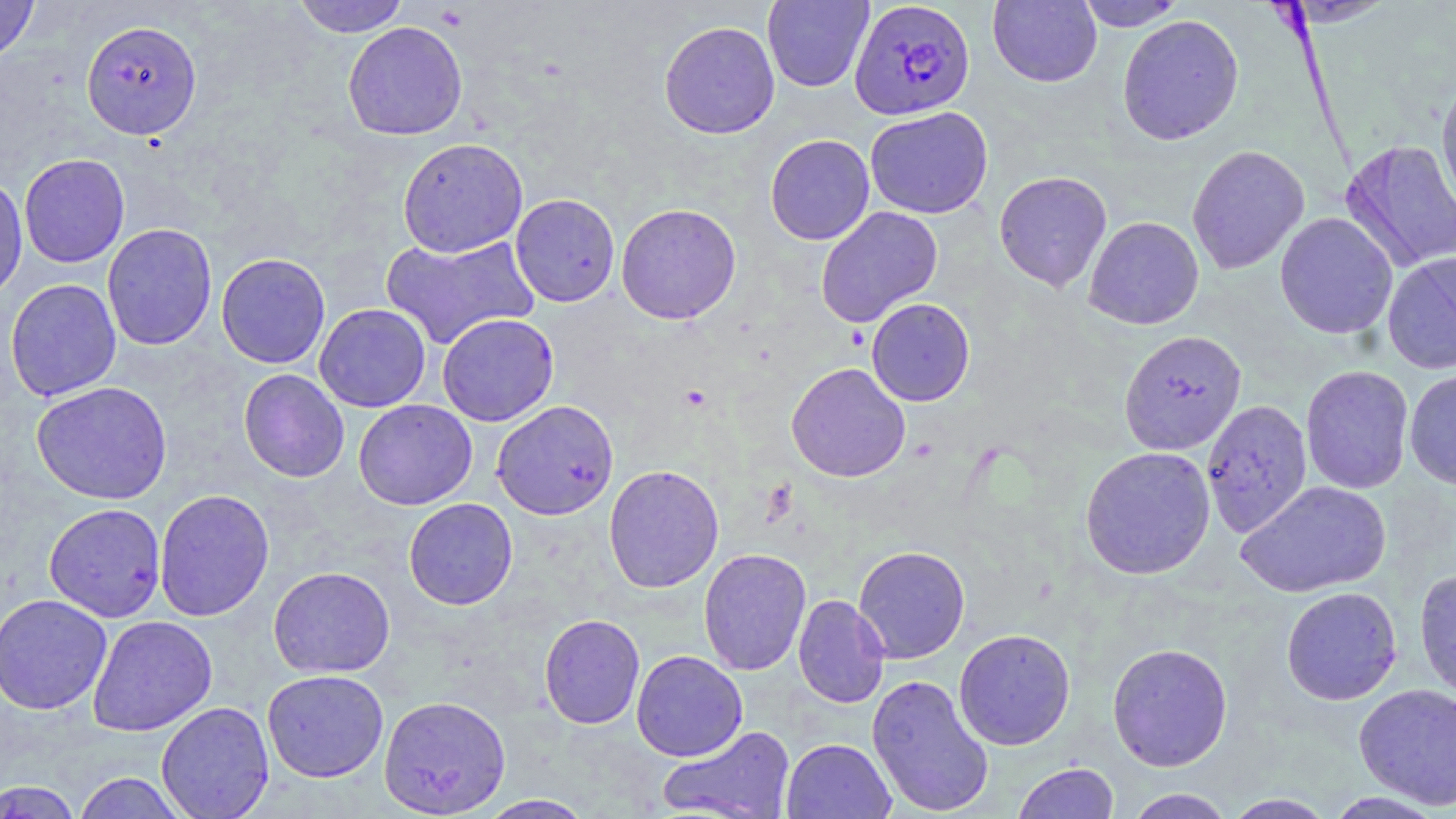
Summary:
  - Coordinate format: approximate bounding boxes as named x1/y1/x2/y2 corners in pixels
  - Plasmodium falciparum-infected red blood cell locations: (x1=849, y1=1, x2=976, y2=120)
  - Uninfected red blood cell locations: (x1=0, y1=0, x2=39, y2=66), (x1=292, y1=0, x2=410, y2=37), (x1=762, y1=0, x2=873, y2=92), (x1=1075, y1=0, x2=1187, y2=31), (x1=987, y1=1, x2=1101, y2=88), (x1=1281, y1=1, x2=1397, y2=27), (x1=1117, y1=15, x2=1244, y2=145), (x1=81, y1=20, x2=202, y2=140), (x1=342, y1=21, x2=468, y2=141), (x1=659, y1=21, x2=780, y2=139), (x1=1436, y1=75, x2=1456, y2=216), (x1=865, y1=106, x2=993, y2=219), (x1=765, y1=134, x2=875, y2=245), (x1=397, y1=137, x2=528, y2=258), (x1=1341, y1=139, x2=1456, y2=272), (x1=1187, y1=144, x2=1309, y2=274), (x1=19, y1=153, x2=130, y2=268), (x1=993, y1=171, x2=1112, y2=292), (x1=0, y1=174, x2=28, y2=301), (x1=510, y1=193, x2=621, y2=307), (x1=616, y1=203, x2=741, y2=324), (x1=815, y1=206, x2=943, y2=327), (x1=1274, y1=212, x2=1398, y2=339), (x1=1084, y1=216, x2=1204, y2=330), (x1=101, y1=223, x2=217, y2=350), (x1=379, y1=233, x2=540, y2=350), (x1=215, y1=252, x2=331, y2=369), (x1=1382, y1=252, x2=1456, y2=374), (x1=5, y1=278, x2=122, y2=402), (x1=866, y1=298, x2=975, y2=406), (x1=314, y1=303, x2=431, y2=412), (x1=436, y1=313, x2=559, y2=426), (x1=1119, y1=330, x2=1246, y2=455), (x1=786, y1=362, x2=910, y2=482), (x1=1300, y1=365, x2=1414, y2=494), (x1=1404, y1=368, x2=1456, y2=490), (x1=238, y1=369, x2=349, y2=483), (x1=31, y1=381, x2=173, y2=505), (x1=1201, y1=399, x2=1312, y2=538), (x1=353, y1=400, x2=477, y2=510), (x1=491, y1=400, x2=619, y2=520), (x1=1080, y1=446, x2=1215, y2=580), (x1=603, y1=465, x2=724, y2=593), (x1=1235, y1=480, x2=1392, y2=599), (x1=154, y1=489, x2=275, y2=621), (x1=403, y1=498, x2=518, y2=610), (x1=44, y1=502, x2=166, y2=621), (x1=853, y1=545, x2=970, y2=663), (x1=698, y1=547, x2=812, y2=676), (x1=268, y1=566, x2=395, y2=678), (x1=1414, y1=566, x2=1456, y2=701), (x1=1280, y1=587, x2=1403, y2=705), (x1=0, y1=593, x2=112, y2=715), (x1=793, y1=594, x2=889, y2=709), (x1=539, y1=613, x2=645, y2=729), (x1=87, y1=615, x2=217, y2=736), (x1=953, y1=628, x2=1075, y2=750), (x1=1107, y1=642, x2=1233, y2=771), (x1=631, y1=650, x2=747, y2=761), (x1=262, y1=669, x2=389, y2=782), (x1=867, y1=674, x2=994, y2=816), (x1=1353, y1=683, x2=1456, y2=809), (x1=379, y1=695, x2=511, y2=817), (x1=156, y1=701, x2=274, y2=819), (x1=657, y1=725, x2=796, y2=819), (x1=781, y1=738, x2=896, y2=819), (x1=1012, y1=762, x2=1120, y2=818), (x1=72, y1=772, x2=188, y2=818), (x1=0, y1=780, x2=84, y2=818), (x1=1123, y1=788, x2=1235, y2=818), (x1=1325, y1=791, x2=1447, y2=818), (x1=1222, y1=793, x2=1337, y2=818), (x1=474, y1=794, x2=597, y2=818)
  - Platelet locations: (x1=681, y1=384, x2=711, y2=411)
  - Slide-level diagnosis: Plasmodium falciparum
  - Preparation: thin blood film
  - Image size: 1456×819 pixels
  - Field of view: single
  - Stain: May-Grünwald-Giemsa
  - Modality: optical microscopy
  - Magnification: 1000x